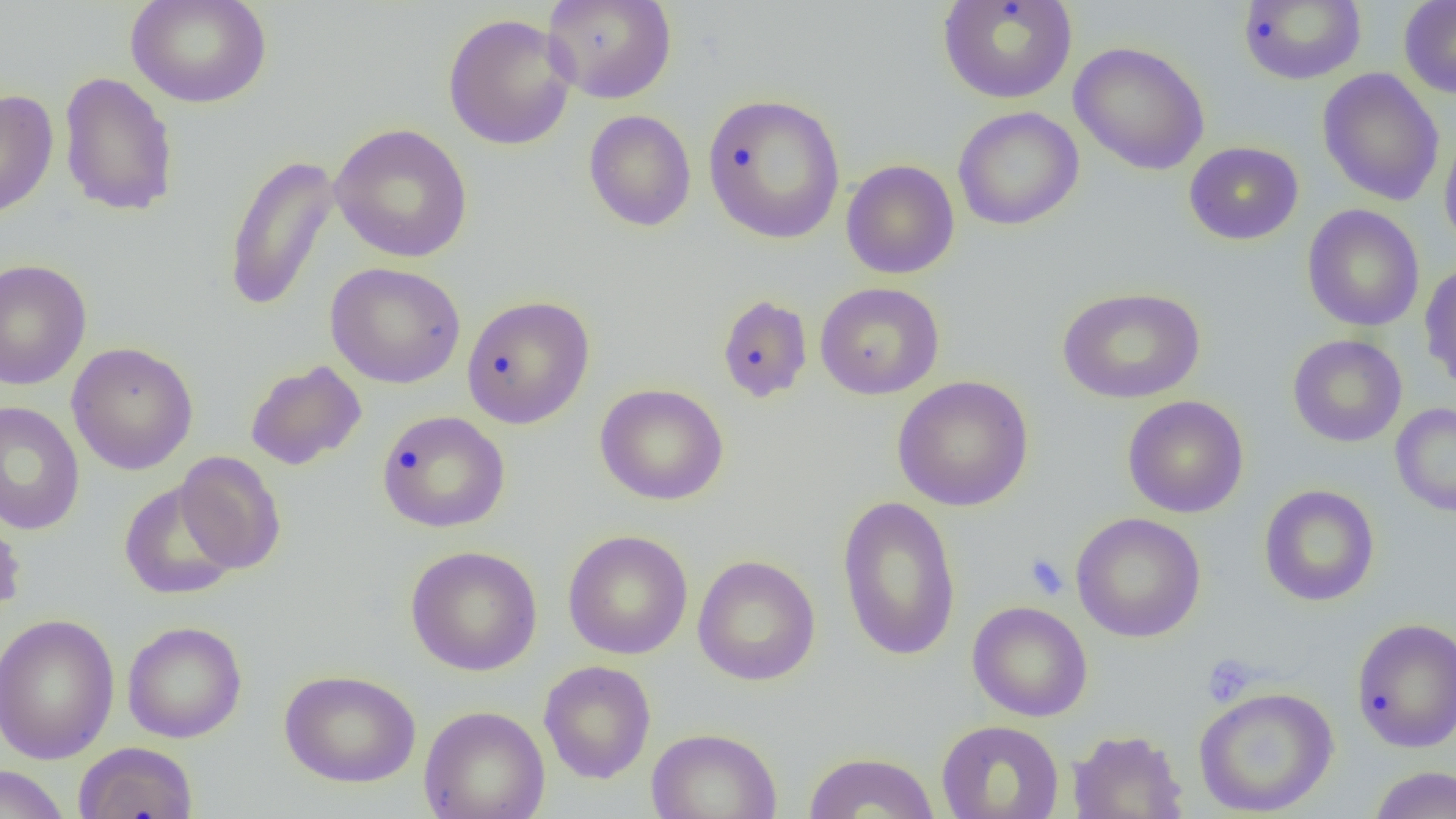
Summary:
  - Coordinate format: approximate bounding boxes as named x1/y1/x2/y2 corners in pixels
  - Uninfected red blood cell locations: (x1=125, y1=0, x2=273, y2=109), (x1=542, y1=0, x2=677, y2=104), (x1=937, y1=0, x2=1077, y2=104), (x1=1238, y1=0, x2=1366, y2=85), (x1=1398, y1=0, x2=1456, y2=99), (x1=442, y1=12, x2=578, y2=151), (x1=1069, y1=40, x2=1210, y2=176), (x1=1317, y1=68, x2=1445, y2=207), (x1=58, y1=71, x2=180, y2=217), (x1=0, y1=88, x2=58, y2=220), (x1=702, y1=90, x2=846, y2=241), (x1=952, y1=106, x2=1084, y2=231), (x1=584, y1=109, x2=697, y2=232), (x1=329, y1=123, x2=473, y2=263), (x1=1439, y1=123, x2=1456, y2=255), (x1=1184, y1=141, x2=1303, y2=246), (x1=223, y1=152, x2=341, y2=313), (x1=841, y1=159, x2=960, y2=279), (x1=1302, y1=204, x2=1425, y2=332), (x1=0, y1=259, x2=92, y2=391), (x1=1419, y1=260, x2=1456, y2=390), (x1=325, y1=262, x2=466, y2=388), (x1=815, y1=282, x2=944, y2=400), (x1=1057, y1=286, x2=1206, y2=404), (x1=716, y1=293, x2=813, y2=404), (x1=461, y1=294, x2=595, y2=429), (x1=1287, y1=334, x2=1408, y2=447), (x1=66, y1=341, x2=199, y2=475), (x1=245, y1=359, x2=367, y2=471), (x1=892, y1=375, x2=1034, y2=511), (x1=595, y1=383, x2=730, y2=505), (x1=1122, y1=395, x2=1249, y2=518), (x1=0, y1=401, x2=85, y2=536), (x1=1390, y1=402, x2=1456, y2=517), (x1=376, y1=410, x2=511, y2=533), (x1=174, y1=451, x2=286, y2=574), (x1=119, y1=480, x2=242, y2=600), (x1=1259, y1=485, x2=1380, y2=607), (x1=837, y1=494, x2=961, y2=662), (x1=0, y1=507, x2=26, y2=627), (x1=1070, y1=512, x2=1206, y2=642), (x1=563, y1=529, x2=693, y2=659), (x1=405, y1=545, x2=543, y2=677), (x1=692, y1=554, x2=821, y2=686), (x1=967, y1=600, x2=1093, y2=722), (x1=0, y1=614, x2=120, y2=764), (x1=1351, y1=617, x2=1456, y2=752), (x1=122, y1=621, x2=247, y2=743), (x1=538, y1=660, x2=656, y2=784), (x1=279, y1=669, x2=421, y2=788), (x1=1193, y1=685, x2=1340, y2=817), (x1=419, y1=705, x2=550, y2=819), (x1=936, y1=719, x2=1065, y2=819), (x1=646, y1=727, x2=782, y2=819), (x1=1068, y1=729, x2=1188, y2=818), (x1=73, y1=741, x2=198, y2=819), (x1=804, y1=751, x2=939, y2=818), (x1=0, y1=764, x2=70, y2=819), (x1=1367, y1=765, x2=1456, y2=819)
  - Platelet locations: (x1=1025, y1=553, x2=1069, y2=600), (x1=1201, y1=654, x2=1258, y2=707)
  - Slide-level diagnosis: negative for blood parasites
  - Field of view: one of a larger specimen
  - Modality: optical microscopy
  - Preparation: thin blood film
  - Image size: 1456×819 pixels
  - Magnification: 1000x